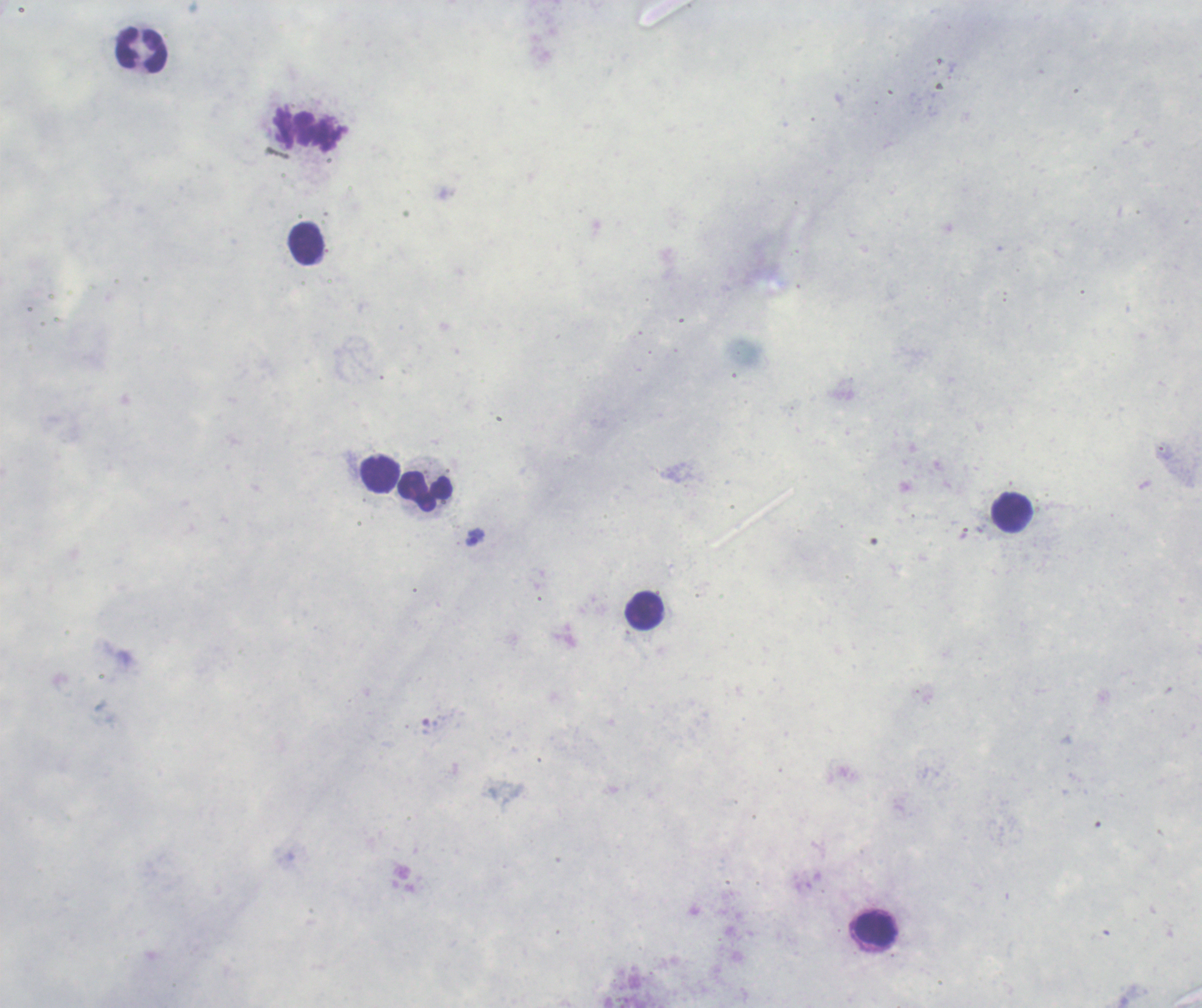
Approximate centers as [x, y] in pixels.
Summary:
  - Trophozoite locations: [476, 537]
  - Leukocyte locations: [142, 50], [306, 244], [381, 475], [425, 491], [1012, 513], [645, 610], [876, 929]
  - Stain: Romanowsky
  - Field of view: one from this slide
  - Result: positive for malaria parasites
  - Magnification: 100x
  - Background quality: poor
  - Context: previously used in a real diagnosis
  - Image size: 1202×1008 pixels
  - Preparation: thick smear of blood